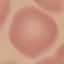

Summary:
  - Malaria status: uninfected
  - Preparation: thin blood film
  - Capture: smartphone camera at the microscope eyepiece
  - Stain: Giemsa
  - Image type: cell patch, automatically extracted from a larger field of view and resized to 64 × 64 pixels